Give the position of each Plasmodium falciparum parasite with its life-cycle stage, each leukocyte, and any debris.
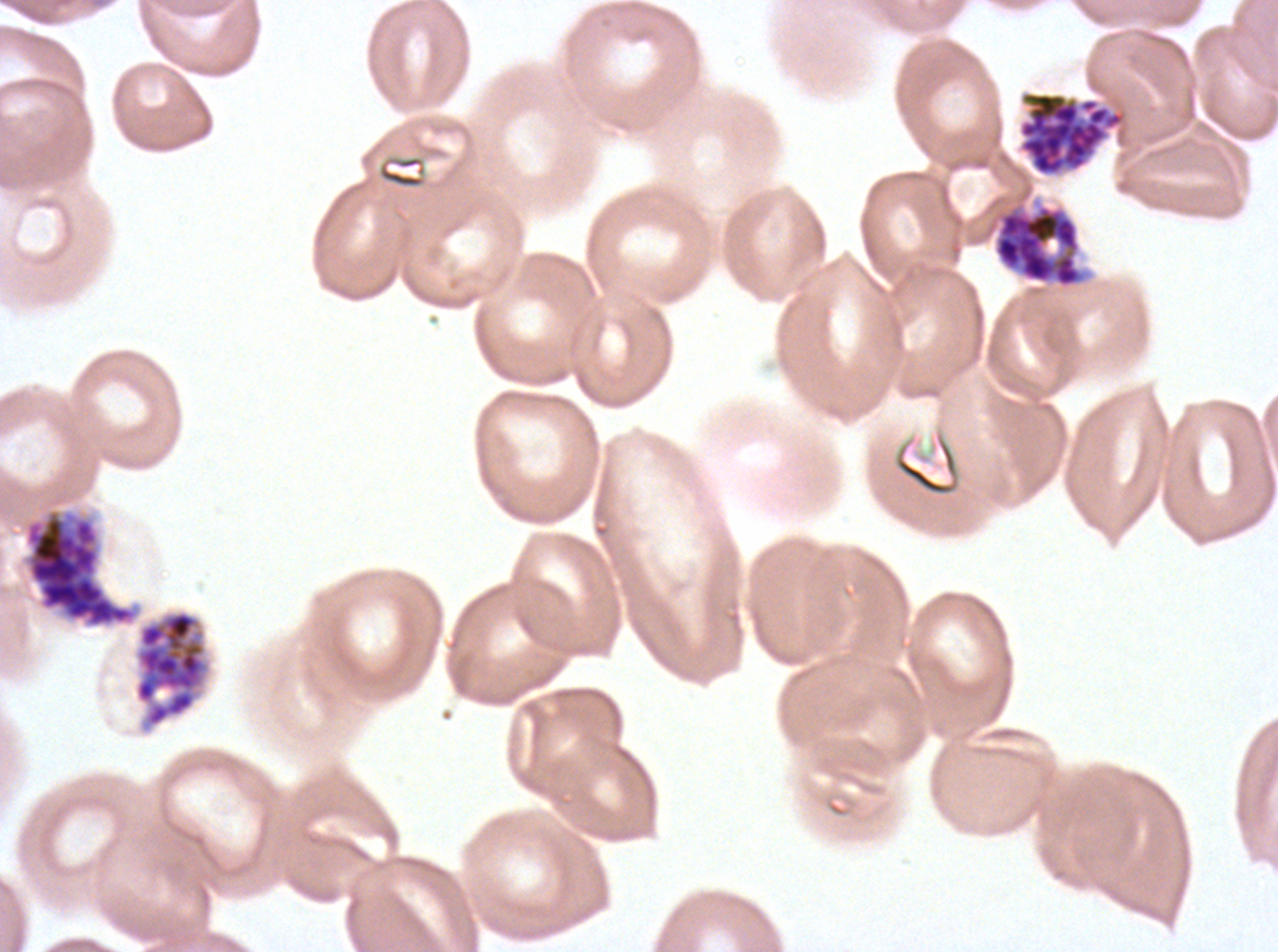
Approximate bounding boxes as [x1, y1, x2, y2] in pixels.
Late schizonts: [134, 609, 210, 727].
Segmenters: [1018, 92, 1125, 176], [992, 201, 1088, 289], [23, 507, 140, 629].
No rings, late-ring/early-trophozoite forms, mid trophozoites, late trophozoites, early schizonts, gametocytes, leukocytes, or debris observed.

Summary:
  - Preparation: thin blood film
  - Life-cycle stages observed: late schizont, segmenter
  - Field of view: sub-image separated from a larger composite
  - Image size: 1278×952 pixels
  - Specimen: ex-vivo Plasmodium falciparum culture from a patient in The Gambia, grown for 24 to 48 hours
  - Stain: Giemsa